Identify the parasite.
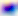
Toxoplasma gondii.

Summary:
  - Modality: photomicrograph
  - Magnification: 400x